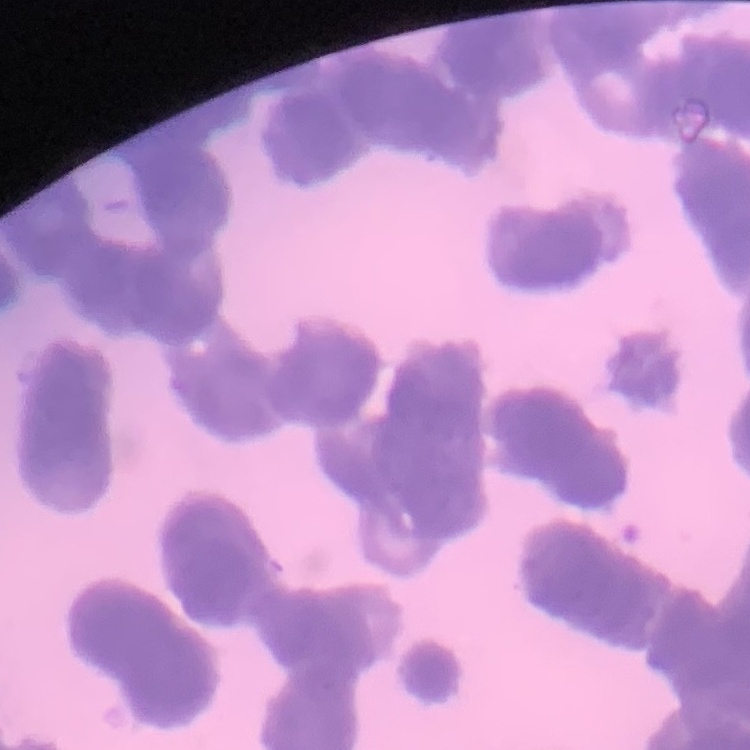 The red blood cells exhibit rouleaux formation. Thin blood film. Field's or Giemsa stain. Square crop of a larger photomicrograph.